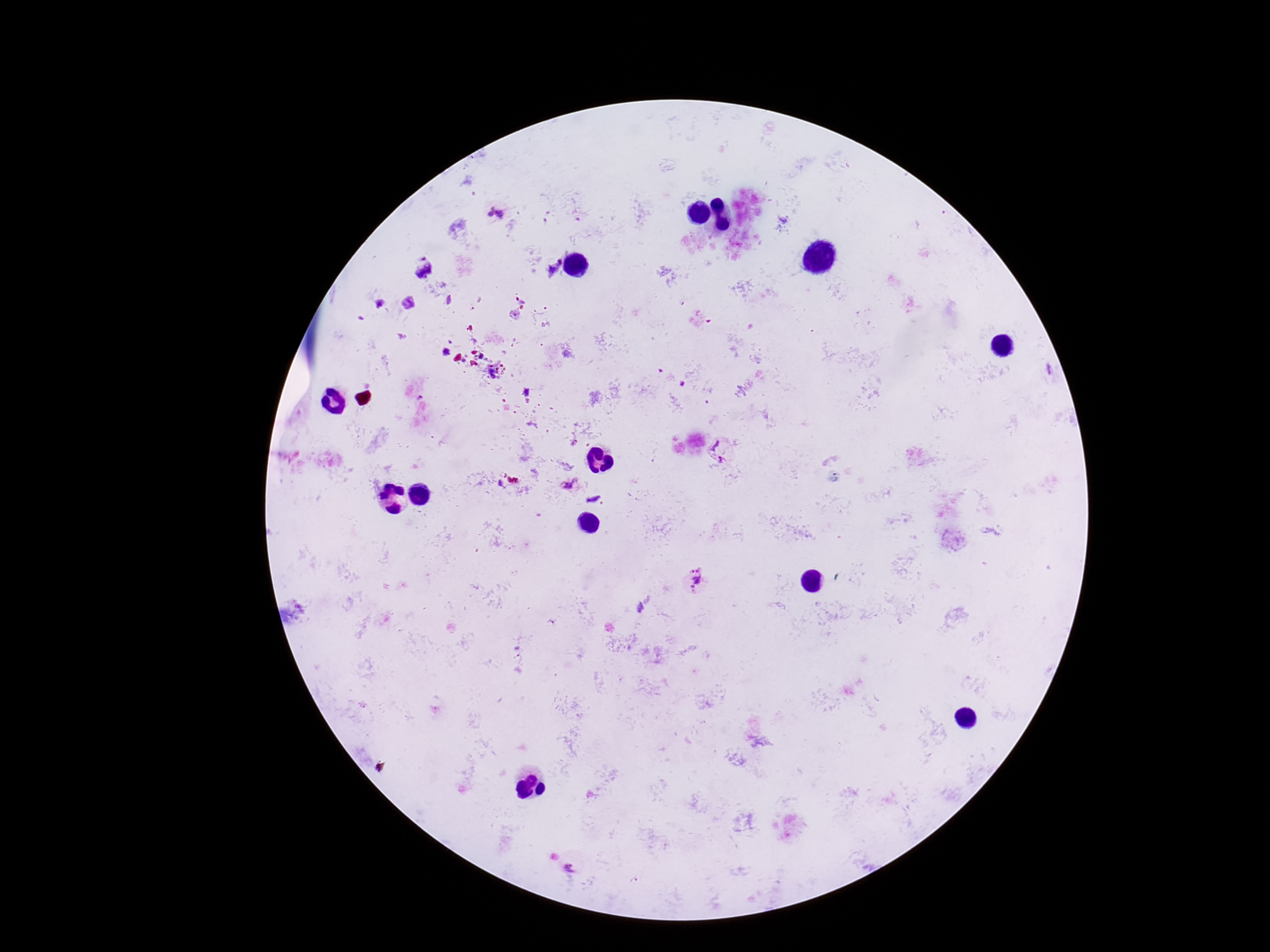

magnification: 100x
stain: Giemsa
capture: smartphone camera through the microscope eyepiece
field_of_view: one from this slide
image_size: 1270×952 pixels
preparation: thick blood smear
plasmodium_parasite_locations: 'approximate object centers, in pixels from the top-left corner: (x=497, y=214), (x=419, y=265), (x=518, y=294), (x=721, y=449), (x=568, y=485), (x=695, y=580)'
patient_malaria_status: infected